Assess the morphology of the erythrocytes.
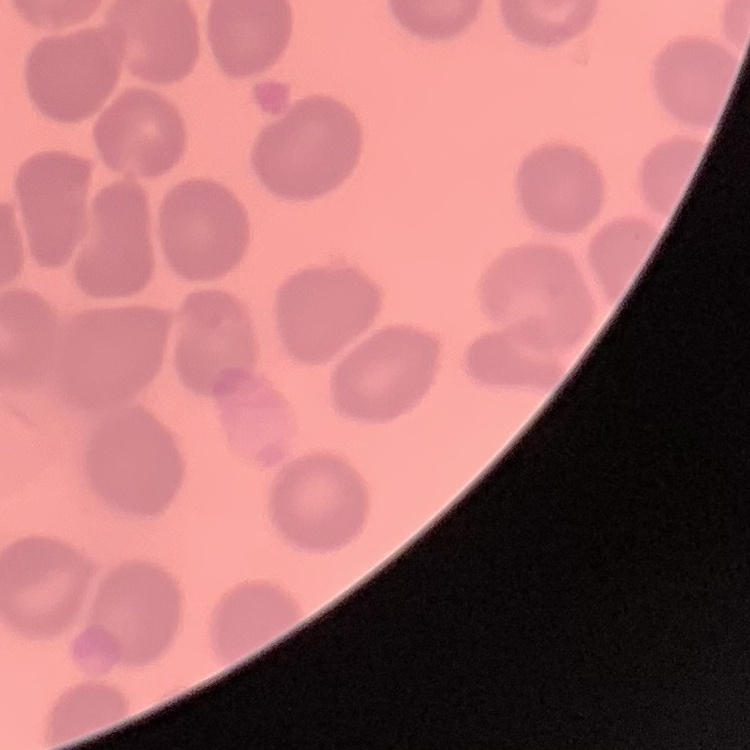
They show no rouleaux formation.

stain = Field's or Giemsa
preparation = thin blood film
image type = square crop of a larger photomicrograph